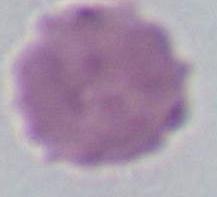
Summary:
  - Identification: erythrocyte
  - Modality: photomicrograph
  - Magnification: 1000x